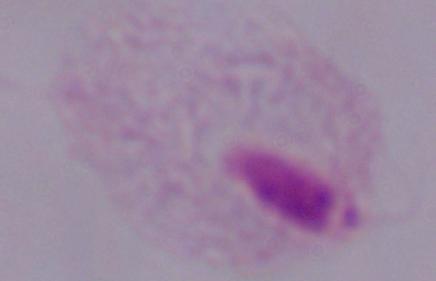
1000x magnification. A trichomonad is shown. Micrograph.